Name the cell type shown.
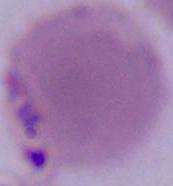
An erythrocyte.

{
  "modality": "photomicrograph",
  "magnification": "1000x"
}